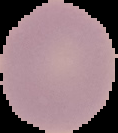
Image is 118×133 pixels. From a thin blood smear. Malaria status: uninfected. Cell region segmented out of the field of view; the surrounding area is masked to black.